Identify the preparation type.
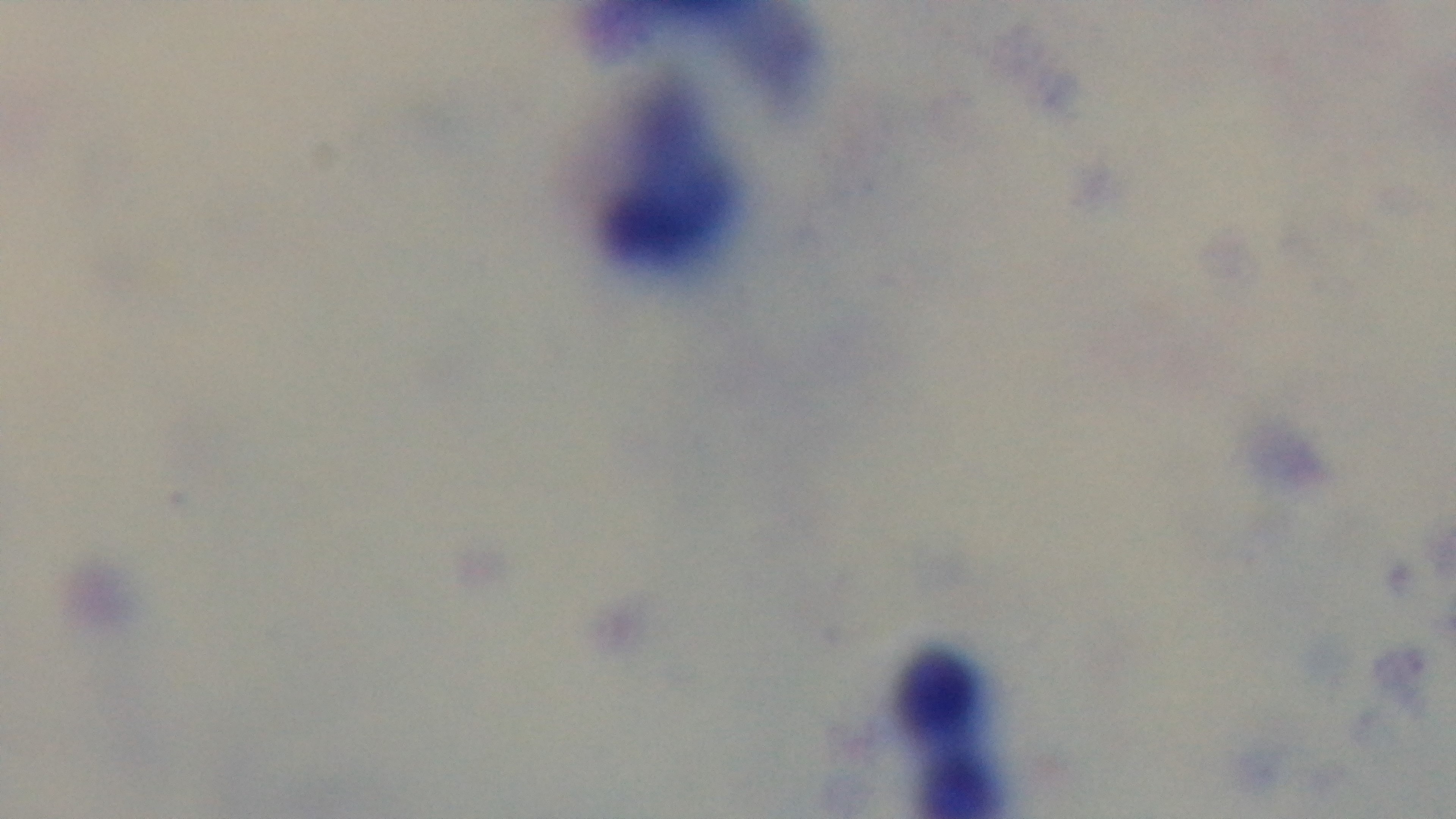
A thick smear.

Photomicrograph. Malaria status: uninfected. One field from the slide. Oil-immersion objective, 100x. Giemsa-stained. Mounted 4K digital camera.